Assess the morphology of the red blood cells.
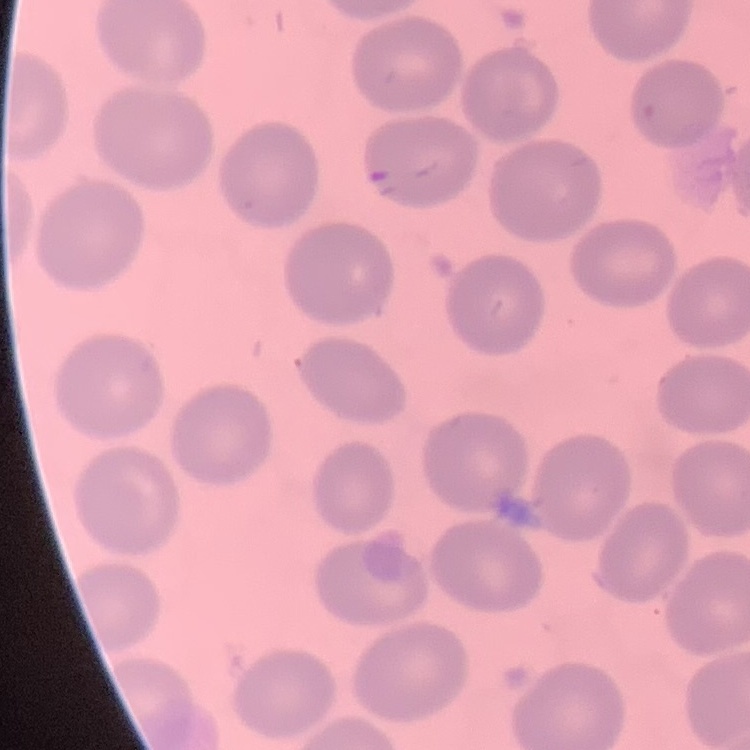

No rouleaux formation.

Summary:
  - Preparation: thin peripheral smear
  - Stain: Field's or Giemsa
  - Image type: square crop of a larger photomicrograph